Outline each blood parasite and name the species.
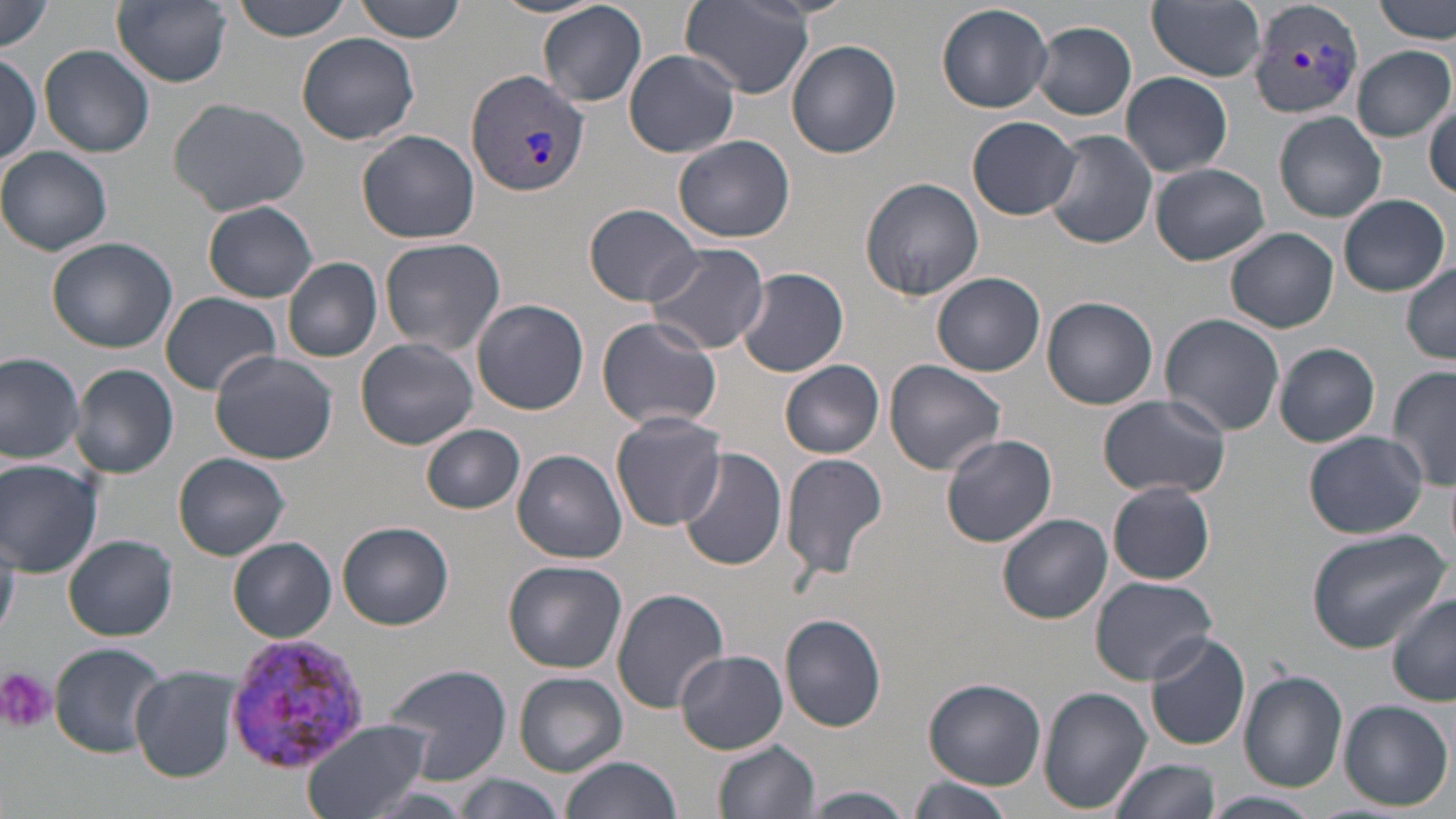
Approximate bounding boxes as named x1/y1/x2/y2 corners in pixels.
Plasmodium vivax-infected red blood cells: (x1=1247, y1=0, x2=1365, y2=121), (x1=467, y1=67, x2=588, y2=199), (x1=223, y1=634, x2=374, y2=775).
No Plasmodium falciparum, Plasmodium ovale, Plasmodium malariae, Babesia divergens, or Trypanosoma brucei observed.

slide-level diagnosis = Plasmodium vivax
image size = 1456×819 pixels
platelet locations = approximate bounding boxes as named x1/y1/x2/y2 corners in pixels: (x1=0, y1=667, x2=54, y2=731)
uninfected red blood cell locations = approximate bounding boxes as named x1/y1/x2/y2 corners in pixels: (x1=113, y1=0, x2=231, y2=87), (x1=227, y1=0, x2=355, y2=42), (x1=354, y1=0, x2=468, y2=43), (x1=493, y1=0, x2=608, y2=20), (x1=679, y1=0, x2=818, y2=97), (x1=1148, y1=0, x2=1266, y2=82), (x1=1375, y1=0, x2=1454, y2=44), (x1=0, y1=1, x2=54, y2=54), (x1=537, y1=2, x2=648, y2=107), (x1=935, y1=3, x2=1053, y2=112), (x1=1030, y1=21, x2=1137, y2=120), (x1=297, y1=32, x2=420, y2=146), (x1=786, y1=39, x2=902, y2=159), (x1=41, y1=45, x2=155, y2=160), (x1=1353, y1=45, x2=1454, y2=142), (x1=623, y1=49, x2=741, y2=158), (x1=0, y1=55, x2=44, y2=164), (x1=1121, y1=72, x2=1232, y2=177), (x1=168, y1=97, x2=311, y2=216), (x1=1426, y1=103, x2=1456, y2=201), (x1=1274, y1=112, x2=1387, y2=222), (x1=967, y1=115, x2=1081, y2=220), (x1=356, y1=128, x2=479, y2=244), (x1=1042, y1=130, x2=1158, y2=250), (x1=672, y1=135, x2=796, y2=243), (x1=0, y1=146, x2=115, y2=256), (x1=1149, y1=162, x2=1270, y2=266), (x1=858, y1=176, x2=984, y2=302), (x1=1338, y1=194, x2=1452, y2=296), (x1=203, y1=201, x2=318, y2=303), (x1=582, y1=203, x2=702, y2=305), (x1=1226, y1=227, x2=1339, y2=332), (x1=47, y1=236, x2=177, y2=353), (x1=378, y1=237, x2=507, y2=355), (x1=644, y1=241, x2=769, y2=354), (x1=282, y1=257, x2=382, y2=362), (x1=1402, y1=262, x2=1456, y2=361), (x1=737, y1=268, x2=849, y2=379), (x1=933, y1=272, x2=1046, y2=377), (x1=159, y1=292, x2=282, y2=396), (x1=1042, y1=294, x2=1158, y2=410), (x1=472, y1=299, x2=589, y2=415), (x1=1159, y1=313, x2=1285, y2=435), (x1=594, y1=317, x2=724, y2=430), (x1=356, y1=338, x2=479, y2=449), (x1=1274, y1=343, x2=1381, y2=447), (x1=209, y1=350, x2=337, y2=465), (x1=0, y1=353, x2=84, y2=463), (x1=883, y1=360, x2=1006, y2=476), (x1=779, y1=361, x2=883, y2=458), (x1=71, y1=363, x2=179, y2=478), (x1=1386, y1=365, x2=1456, y2=492), (x1=1099, y1=396, x2=1233, y2=499), (x1=609, y1=413, x2=727, y2=532), (x1=422, y1=424, x2=525, y2=514), (x1=1303, y1=431, x2=1428, y2=538), (x1=939, y1=433, x2=1057, y2=548), (x1=680, y1=447, x2=791, y2=573), (x1=513, y1=449, x2=627, y2=563), (x1=780, y1=452, x2=888, y2=581), (x1=174, y1=453, x2=290, y2=560), (x1=0, y1=460, x2=103, y2=577), (x1=1108, y1=481, x2=1216, y2=585), (x1=998, y1=512, x2=1113, y2=624), (x1=337, y1=520, x2=455, y2=630), (x1=0, y1=526, x2=20, y2=636), (x1=1304, y1=526, x2=1450, y2=651), (x1=63, y1=534, x2=179, y2=640), (x1=227, y1=537, x2=336, y2=642), (x1=504, y1=560, x2=627, y2=673), (x1=1090, y1=576, x2=1218, y2=684), (x1=611, y1=588, x2=729, y2=714), (x1=1387, y1=596, x2=1456, y2=706), (x1=780, y1=614, x2=887, y2=732), (x1=1143, y1=632, x2=1252, y2=751), (x1=47, y1=644, x2=171, y2=756), (x1=675, y1=649, x2=788, y2=753), (x1=381, y1=664, x2=516, y2=785), (x1=130, y1=665, x2=244, y2=782), (x1=1238, y1=670, x2=1348, y2=791), (x1=514, y1=672, x2=627, y2=776), (x1=921, y1=678, x2=1045, y2=789), (x1=1039, y1=686, x2=1151, y2=813), (x1=1339, y1=699, x2=1452, y2=810), (x1=299, y1=719, x2=432, y2=819), (x1=712, y1=738, x2=821, y2=819), (x1=560, y1=756, x2=683, y2=819), (x1=1109, y1=758, x2=1220, y2=819), (x1=454, y1=776, x2=566, y2=819), (x1=906, y1=777, x2=1014, y2=819), (x1=805, y1=788, x2=917, y2=818), (x1=1204, y1=791, x2=1325, y2=819)
preparation = thin blood smear
field of view = single
modality = light microscopy
magnification = 1000x
stain = May-Grünwald-Giemsa